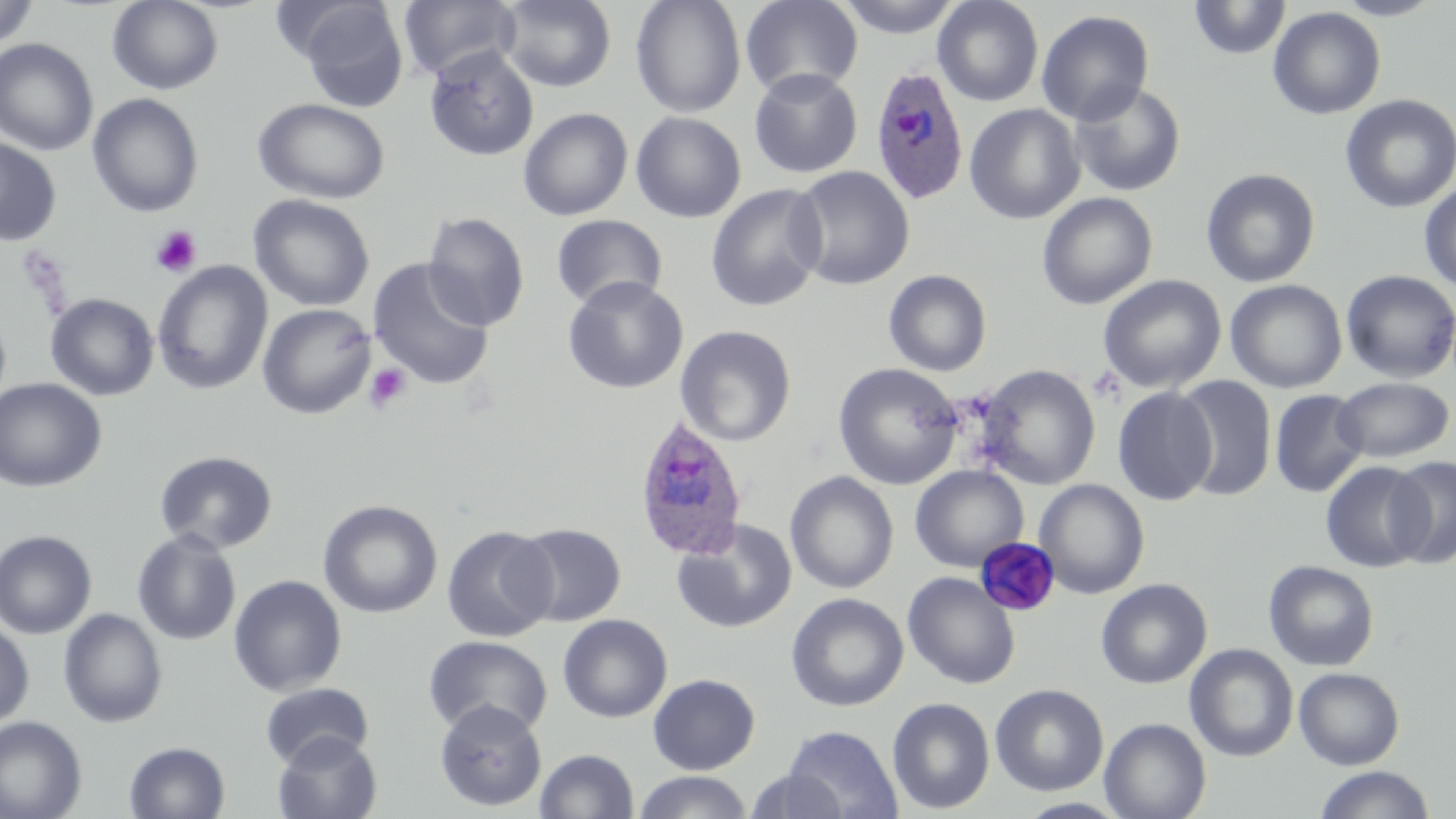 Approximate bounding boxes as [x1, y1, x2, y2] in pixels. Uninfected red blood cell locations: [107, 0, 224, 95], [399, 0, 521, 83], [497, 0, 617, 92], [630, 0, 746, 117], [740, 0, 863, 99], [835, 0, 964, 38], [932, 0, 1044, 107], [1331, 0, 1446, 21], [0, 1, 39, 52], [294, 1, 410, 112], [1188, 1, 1292, 60], [1267, 6, 1386, 120], [1036, 10, 1155, 126], [0, 38, 99, 156], [423, 45, 540, 161], [749, 67, 863, 179], [1068, 82, 1186, 197], [87, 93, 204, 217], [1339, 94, 1456, 214], [253, 98, 391, 204], [964, 104, 1085, 224], [518, 107, 633, 221], [630, 112, 747, 223], [0, 135, 62, 246], [787, 166, 915, 290], [1201, 168, 1320, 288], [1418, 182, 1456, 292], [705, 184, 827, 312], [1037, 192, 1158, 310], [247, 194, 375, 312], [422, 211, 530, 331], [550, 215, 668, 311], [367, 257, 496, 391], [152, 260, 273, 395], [883, 270, 992, 376], [1340, 270, 1456, 383], [1097, 274, 1227, 394], [562, 276, 688, 394], [1225, 280, 1347, 393], [45, 293, 159, 401], [257, 303, 377, 419], [675, 325, 797, 447], [833, 362, 964, 490], [974, 364, 1101, 490], [1172, 376, 1277, 501], [1333, 376, 1455, 463], [0, 377, 107, 492], [1111, 386, 1216, 505], [1270, 390, 1369, 498], [154, 450, 278, 553], [1385, 454, 1456, 569], [1321, 461, 1431, 573], [910, 465, 1029, 572], [785, 471, 899, 594], [1033, 479, 1150, 598], [317, 499, 442, 618], [671, 518, 797, 634], [511, 522, 626, 626], [441, 524, 558, 643], [131, 528, 242, 646], [0, 529, 97, 638], [974, 537, 1061, 617], [1263, 560, 1380, 671], [902, 572, 1021, 689], [229, 574, 347, 695], [1096, 578, 1212, 689], [786, 592, 909, 712], [58, 608, 168, 728], [557, 613, 673, 723], [0, 620, 34, 730], [423, 635, 552, 738], [1185, 643, 1299, 762], [1294, 667, 1404, 770], [647, 673, 760, 775], [259, 681, 374, 768], [990, 683, 1109, 796], [887, 697, 995, 814], [434, 698, 547, 811], [0, 715, 87, 819], [1099, 717, 1211, 819], [782, 725, 904, 819], [273, 732, 382, 819], [123, 741, 230, 819], [534, 749, 639, 819], [1313, 765, 1436, 819], [745, 768, 850, 817], [633, 771, 753, 818]. Platelet locations: [150, 226, 202, 278], [364, 363, 411, 412]. Plasmodium ovale-infected red blood cell locations: [868, 65, 969, 206], [631, 416, 747, 564]. Slide-level diagnosis: Plasmodium ovale. Captured at 1000x magnification. Single field of view. Optical microscopy. May-Grünwald-Giemsa stain. Image is 1456×819 pixels. Thin blood film.